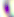

modality = micrograph
magnification = 400x
identification = Toxoplasma gondii